Assess this cell for malaria.
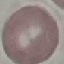
It is uninfected.

Giemsa stain. Automatically extracted cell patch, resized to 64 × 64 pixels. Acquired by smartphone through the microscope eyepiece. Thin blood film.